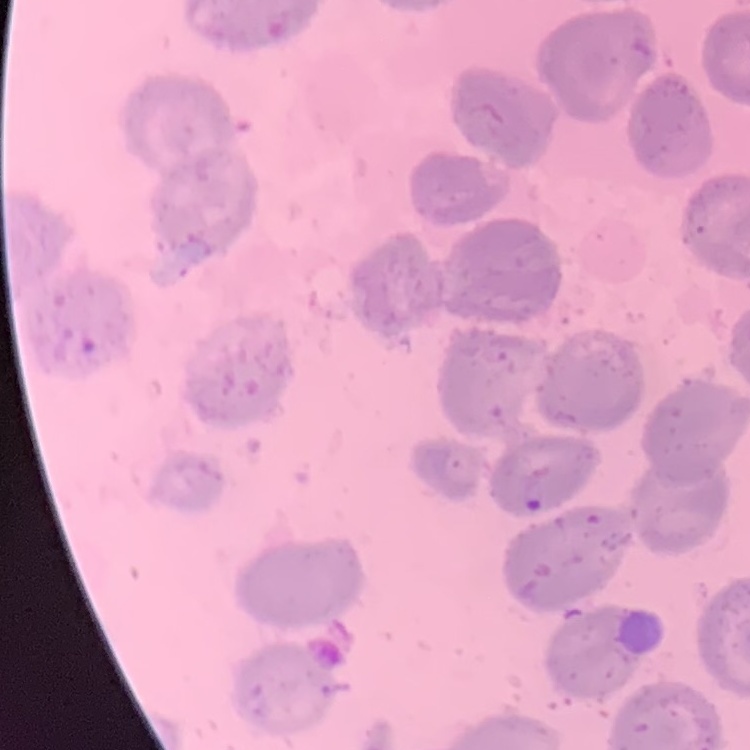

Summary:
  - Erythrocyte morphology: no rouleaux formation
  - Image type: square crop of a larger photomicrograph
  - Stain: Field's or Giemsa
  - Preparation: thin peripheral smear